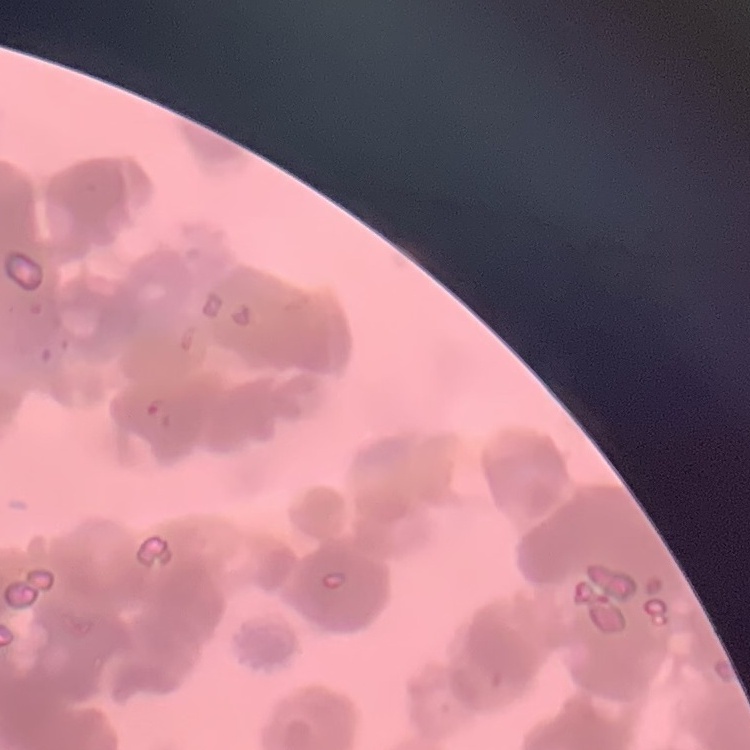
The erythrocytes exhibit rouleaux formation. One tile cut from a larger photomicrograph. Thin blood smear. Field's or Giemsa stain.